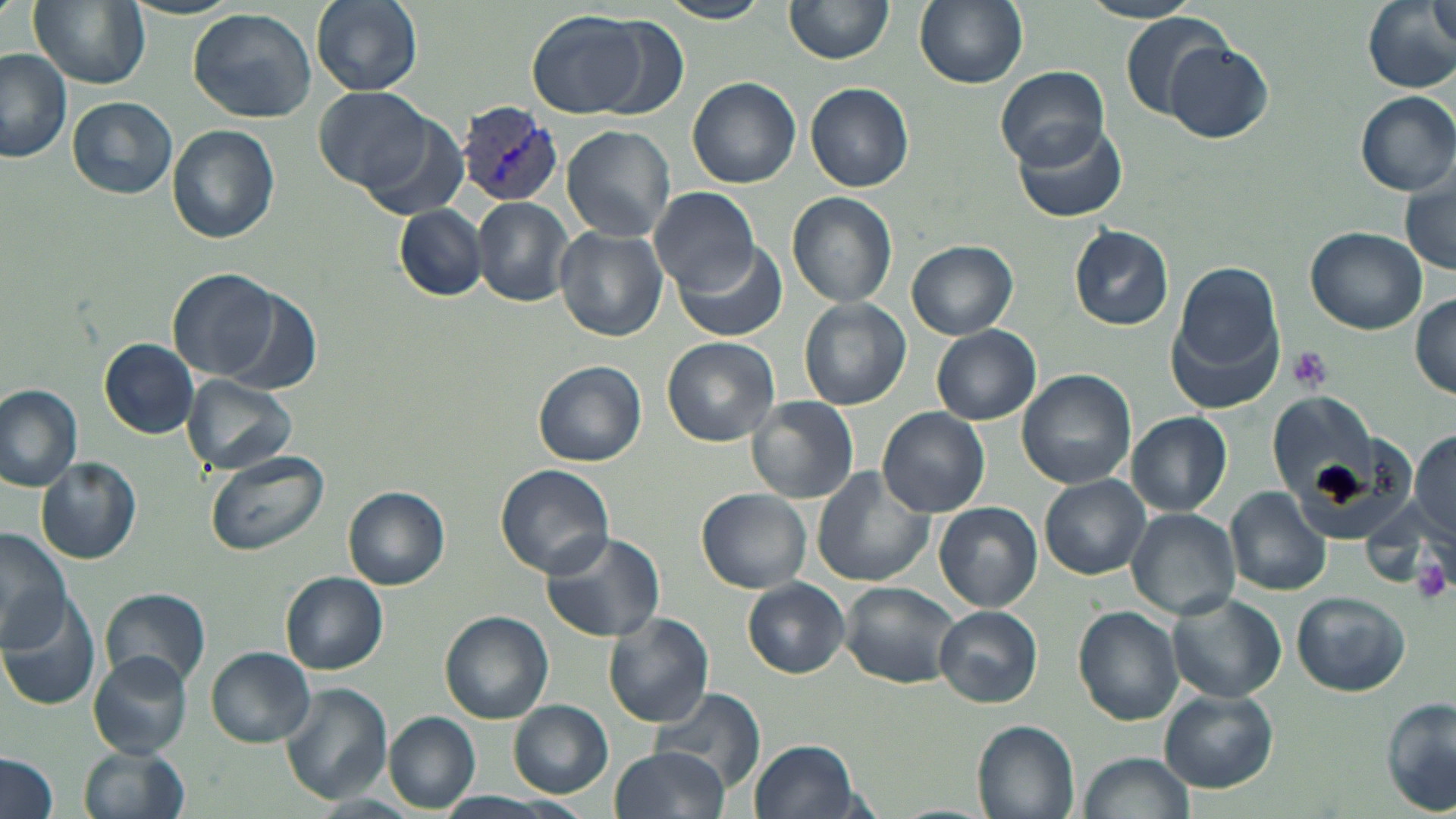 Approximate bounding boxes as (x1, y1, x2, y2) in pixels. Platelet locations: (1288, 345, 1334, 395), (1413, 554, 1452, 604). Uninfected red blood cell locations: (29, 0, 151, 90), (310, 0, 423, 96), (658, 0, 770, 24), (786, 0, 893, 66), (914, 0, 1028, 89), (1078, 0, 1206, 25), (1361, 0, 1455, 95), (1428, 0, 1454, 49), (188, 7, 318, 124), (525, 9, 656, 120), (1121, 12, 1233, 117), (590, 16, 689, 115), (1165, 40, 1273, 143), (0, 49, 73, 163), (996, 69, 1111, 170), (687, 76, 801, 187), (806, 82, 914, 192), (315, 86, 431, 192), (1355, 91, 1456, 195), (67, 96, 178, 199), (355, 110, 470, 221), (1013, 121, 1128, 224), (167, 125, 280, 243), (562, 126, 675, 242), (1400, 164, 1456, 275), (649, 187, 760, 296), (787, 193, 897, 308), (474, 197, 574, 306), (395, 205, 486, 301), (1068, 224, 1173, 330), (1306, 226, 1426, 333), (554, 227, 668, 342), (906, 239, 1018, 340), (673, 240, 789, 343), (1172, 262, 1283, 379), (168, 269, 281, 383), (220, 290, 321, 396), (1411, 293, 1455, 400), (800, 298, 911, 410), (931, 325, 1041, 425), (661, 336, 779, 446), (99, 338, 201, 438), (532, 360, 647, 468), (1017, 369, 1137, 489), (183, 375, 297, 474), (0, 385, 84, 491), (1266, 385, 1403, 529), (746, 396, 859, 504), (878, 407, 990, 516), (1128, 412, 1231, 516), (1411, 428, 1456, 542), (204, 451, 326, 558), (35, 457, 142, 564), (495, 465, 615, 579), (811, 468, 936, 586), (1039, 475, 1151, 579), (345, 486, 449, 589), (698, 488, 814, 594), (1226, 488, 1332, 596), (1360, 499, 1440, 585), (934, 501, 1042, 612), (1126, 508, 1241, 620), (0, 529, 71, 654), (538, 531, 668, 643), (281, 572, 389, 675), (743, 579, 848, 678), (841, 581, 963, 688), (100, 586, 211, 689), (0, 591, 102, 709), (1292, 591, 1411, 695), (1168, 592, 1289, 705), (935, 605, 1043, 708), (1073, 605, 1184, 724), (441, 610, 554, 723), (603, 612, 715, 727), (621, 631, 748, 783), (206, 647, 315, 747), (89, 651, 191, 758), (280, 684, 391, 804), (649, 687, 766, 795), (1160, 689, 1279, 793), (1382, 695, 1456, 815), (508, 700, 613, 797), (384, 713, 479, 812), (971, 718, 1080, 819), (751, 739, 862, 819), (78, 742, 191, 819), (608, 746, 730, 819), (0, 752, 60, 819), (1080, 752, 1193, 819), (426, 792, 570, 818), (309, 795, 418, 818). Plasmodium vivax-infected red blood cell locations: (459, 103, 565, 207). Slide-level diagnosis: Plasmodium vivax. May-Grünwald-Giemsa stain. 1000x magnification. Image is 1456×819 pixels. Light microscopy. One field of a larger specimen. Thin blood film.